Report the malaria status of this cell.
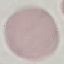
Uninfected.

capture: smartphone through the microscope eyepiece
image_type: cell patch, automatically extracted from a larger field of view and resized to 64 × 64 pixels
stain: Giemsa
preparation: thin blood film